Comment on the morphology of the erythrocytes.
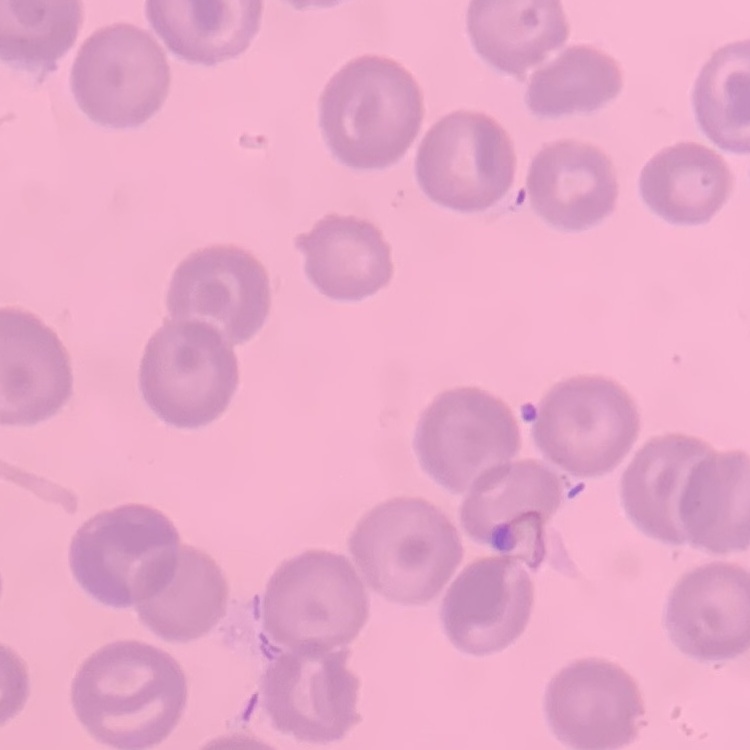
They show no rouleaux formation.

Thin blood film. Stained with either Field's or Giemsa. One tile cut from a larger photomicrograph.